Describe the morphology of the red blood cells.
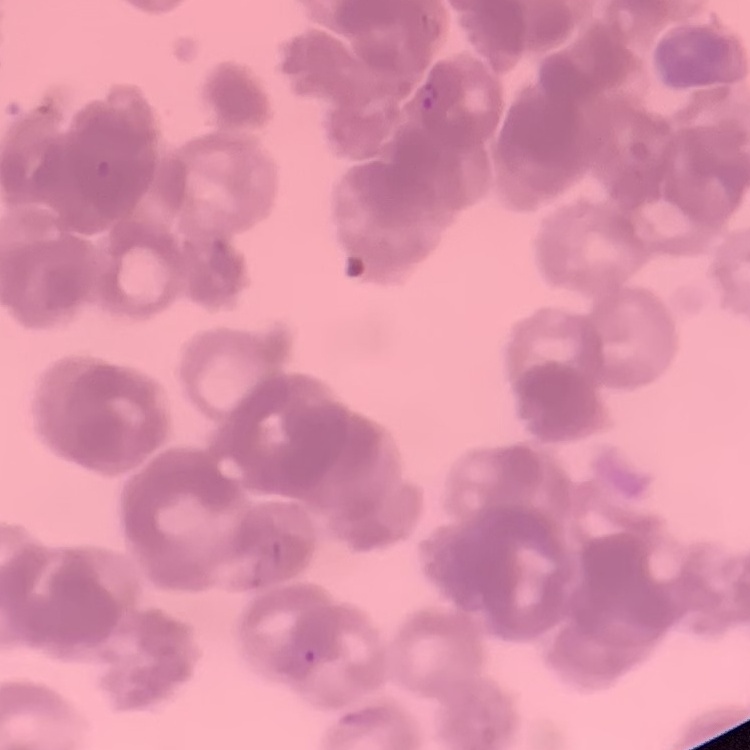
They show rouleaux formation.

Thin peripheral smear. One tile cut from a larger photomicrograph. Field's or Giemsa stain.